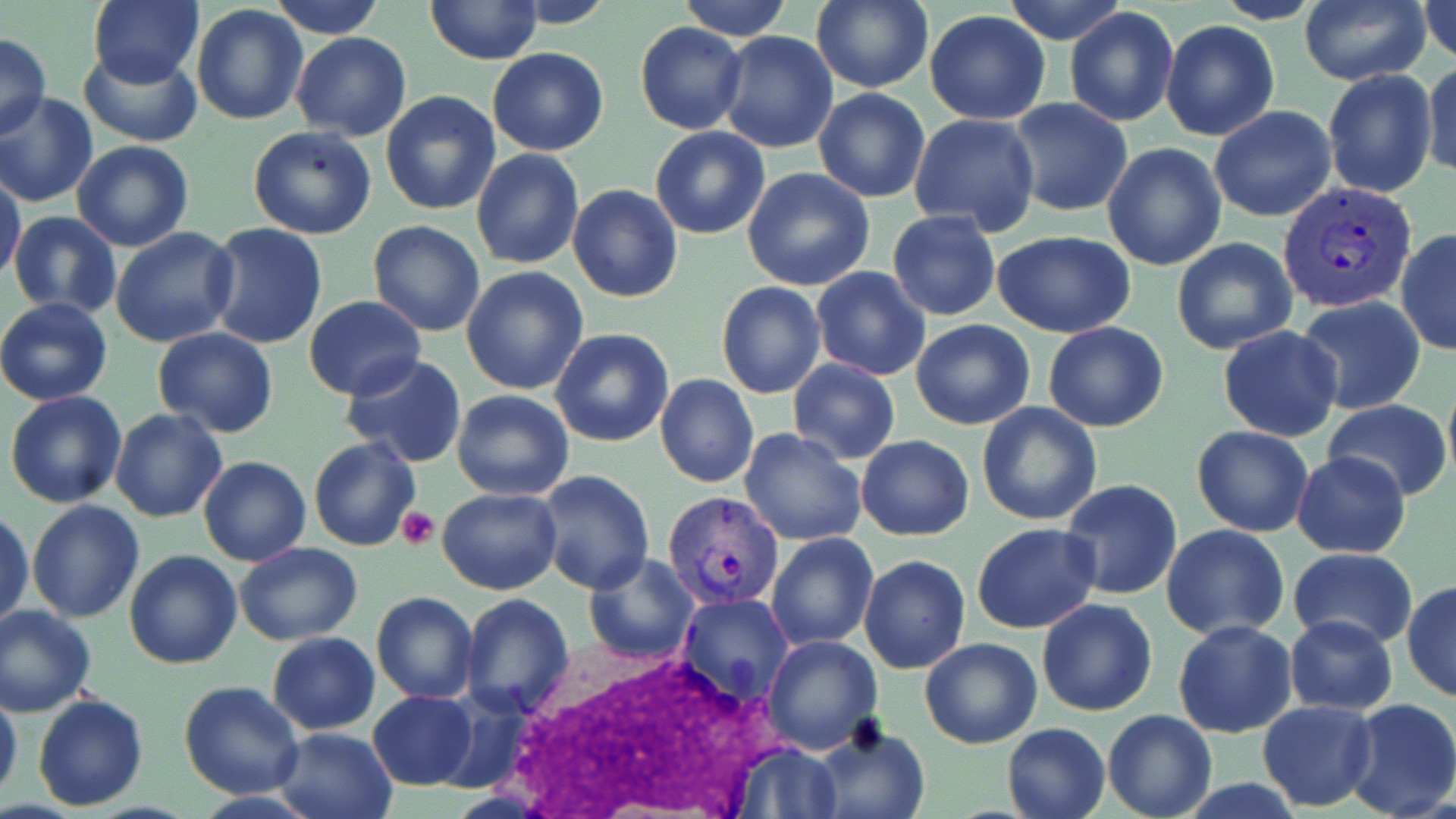

Approximate bounding boxes as [x1, y1, x2, y2] in pixels. Platelet locations: [398, 508, 440, 550]. Uninfected red blood cell locations: [89, 0, 204, 88], [271, 0, 384, 39], [424, 0, 543, 66], [502, 0, 615, 28], [678, 0, 792, 43], [1001, 0, 1130, 45], [1298, 0, 1432, 86], [1418, 0, 1456, 63], [811, 1, 933, 93], [191, 5, 310, 126], [1065, 7, 1179, 127], [922, 11, 1052, 125], [1161, 21, 1279, 140], [635, 23, 747, 134], [291, 32, 411, 141], [716, 32, 837, 153], [0, 34, 50, 139], [79, 47, 201, 146], [487, 48, 608, 157], [1421, 59, 1455, 182], [1323, 69, 1437, 199], [812, 88, 930, 203], [380, 90, 501, 216], [0, 93, 98, 208], [1008, 98, 1132, 216], [1209, 105, 1337, 222], [909, 113, 1040, 237], [248, 125, 378, 239], [650, 126, 771, 240], [71, 140, 194, 252], [595, 141, 725, 279], [1102, 143, 1227, 270], [471, 147, 584, 271], [742, 168, 876, 293], [0, 171, 26, 285], [568, 184, 683, 302], [888, 211, 1000, 320], [8, 212, 123, 319], [368, 220, 486, 336], [205, 224, 328, 350], [112, 227, 241, 348], [1396, 229, 1456, 357], [991, 231, 1139, 338], [1171, 237, 1297, 356], [460, 266, 588, 395], [810, 267, 931, 381], [716, 281, 826, 399], [303, 296, 428, 401], [1296, 296, 1425, 416], [0, 297, 112, 406], [910, 319, 1035, 430], [1043, 321, 1167, 432], [1218, 326, 1344, 442], [550, 328, 674, 446], [152, 329, 278, 437], [340, 352, 467, 468], [787, 359, 901, 465], [655, 374, 759, 489], [451, 390, 574, 500], [6, 391, 128, 510], [1323, 400, 1453, 502], [976, 402, 1103, 526], [110, 409, 227, 524], [1191, 426, 1313, 537], [739, 427, 867, 546], [856, 434, 974, 542], [309, 437, 419, 552], [1292, 450, 1410, 559], [198, 457, 311, 567], [536, 472, 654, 593], [1061, 480, 1183, 601], [438, 489, 563, 594], [26, 500, 144, 622], [0, 509, 34, 633], [973, 523, 1102, 634], [1160, 524, 1290, 641], [767, 533, 878, 650], [236, 543, 364, 645], [1289, 547, 1418, 651], [123, 549, 243, 669], [584, 554, 698, 663], [859, 555, 970, 673], [1403, 581, 1455, 702], [371, 592, 477, 705], [459, 593, 573, 715], [678, 594, 794, 704], [1037, 597, 1158, 717], [0, 605, 97, 716], [1283, 614, 1399, 716], [1172, 619, 1298, 738], [267, 632, 379, 734], [763, 635, 882, 755], [919, 638, 1041, 749], [178, 681, 303, 801], [0, 685, 22, 805], [368, 691, 479, 789], [32, 693, 150, 811], [1343, 698, 1456, 819], [1256, 700, 1379, 811], [1102, 710, 1217, 819], [1000, 722, 1111, 819], [812, 724, 929, 819], [272, 725, 398, 819], [726, 740, 843, 817]. White blood cell locations: [496, 644, 790, 819]. Plasmodium vivax-infected red blood cell locations: [1279, 180, 1421, 313], [661, 490, 784, 610]. Slide-level diagnosis: Plasmodium vivax. May-Grünwald-Giemsa stain. Thin blood film. Captured at 1000x magnification. Image is 1456×819 pixels. Optical microscopy. One field of a larger specimen.